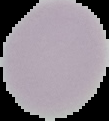

preparation = thin blood smear
image type = segmented cell region with the area outside set to black
image size = 109×121 pixels
result = negative for malaria parasites